Identify the preparation type.
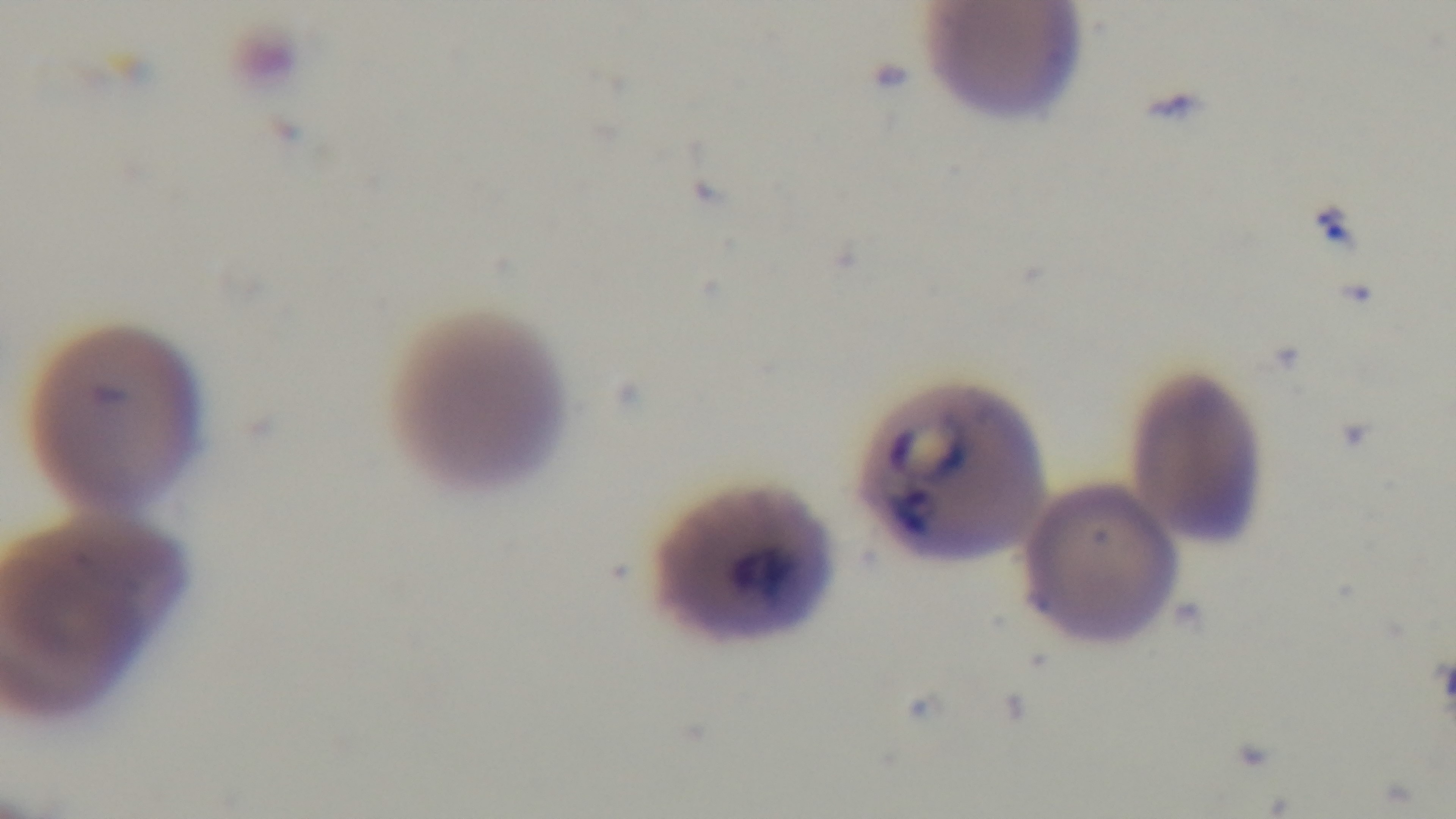
Thin.

objective = 100x oil immersion
capture = mounted 4K digital camera
modality = light microscopy
malaria status = positive
stain = Giemsa
field of view = one from the slide